Draw a bounding box around every malaria parasite.
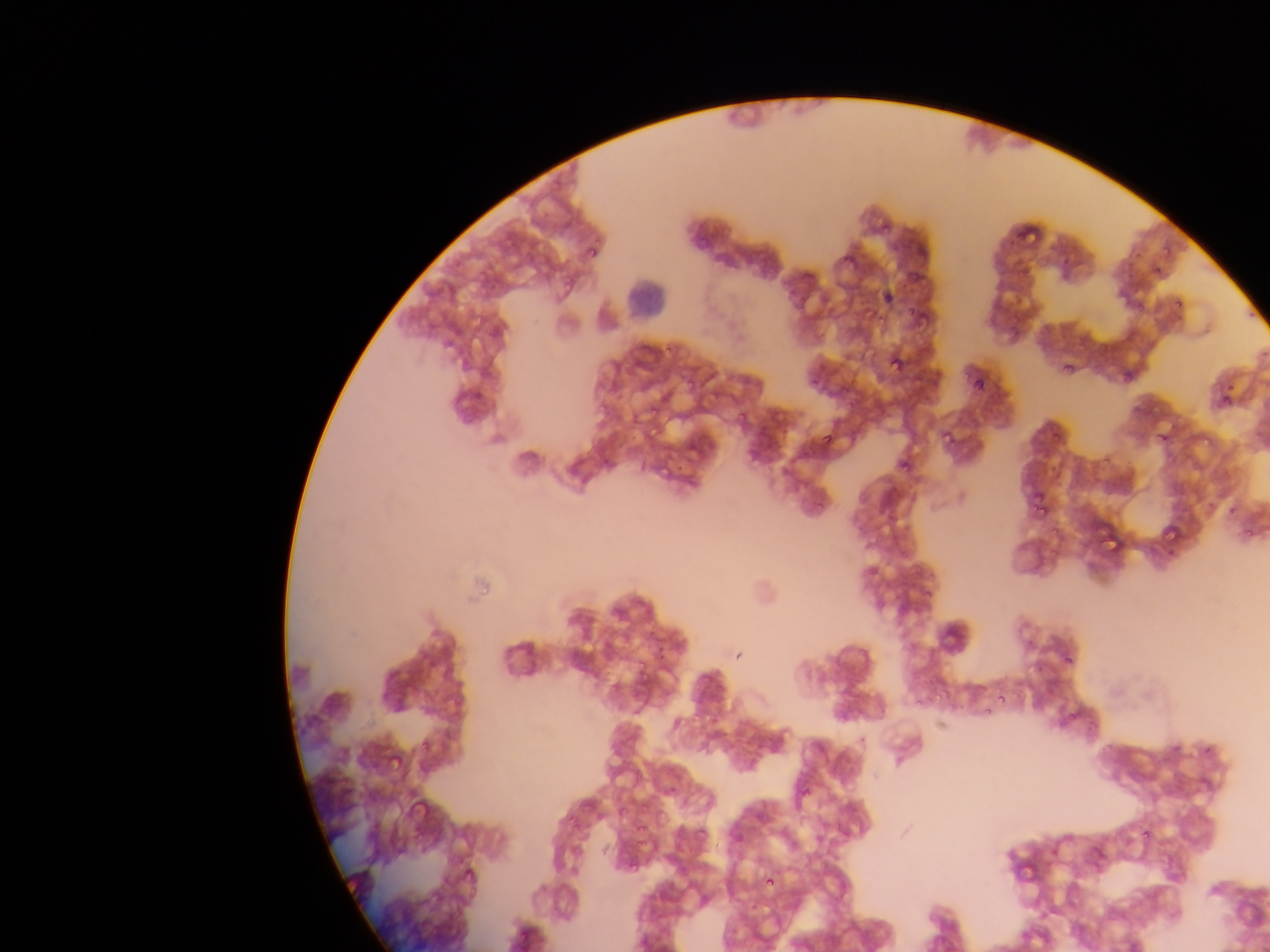

Approximate bounding boxes as {left, top, right, bottom} in pixels.
Malaria parasites: {871, 213, 898, 234}, {1018, 218, 1042, 245}, {694, 226, 714, 243}, {694, 233, 710, 249}, {585, 241, 602, 260}, {1151, 265, 1160, 277}, {882, 289, 897, 302}, {1174, 298, 1184, 308}, {906, 300, 922, 312}, {857, 304, 879, 321}, {888, 353, 904, 372}, {1130, 358, 1145, 377}, {1063, 362, 1075, 373}, {969, 373, 985, 391}, {805, 376, 826, 393}, {1219, 388, 1232, 402}, {709, 389, 721, 397}, {1220, 394, 1232, 407}, {599, 401, 611, 414}, {732, 406, 745, 427}, {649, 423, 664, 437}, {1059, 429, 1068, 436}, {1202, 430, 1223, 446}, {1156, 431, 1170, 445}, {943, 432, 957, 447}, {823, 434, 833, 445}, {1161, 451, 1187, 471}, {897, 458, 911, 473}, {657, 459, 673, 480}, {1030, 491, 1048, 509}, {1033, 498, 1049, 515}, {1164, 523, 1180, 541}, {1243, 523, 1262, 543}, {1096, 536, 1120, 559}, {921, 585, 936, 602}, {1064, 655, 1074, 665}, {631, 664, 647, 690}, {929, 686, 951, 707}, {998, 694, 1007, 703}, {981, 707, 993, 720}, {1064, 709, 1079, 724}, {418, 738, 432, 755}, {1203, 746, 1213, 756}, {631, 767, 643, 780}, {796, 781, 808, 801}, {639, 800, 651, 812}, {565, 814, 579, 829}, {634, 821, 646, 833}, {696, 826, 708, 838}, {1142, 829, 1151, 838}, {763, 874, 777, 888}.

field of view = single
leukocyte locations = approximate bounding boxes as {left, top, right, bottom} in pixels: {621, 271, 665, 319}
preparation = thin blood smear
capture = mobile-phone photograph through a microscope
image size = 1270×952 pixels
country = Ghana